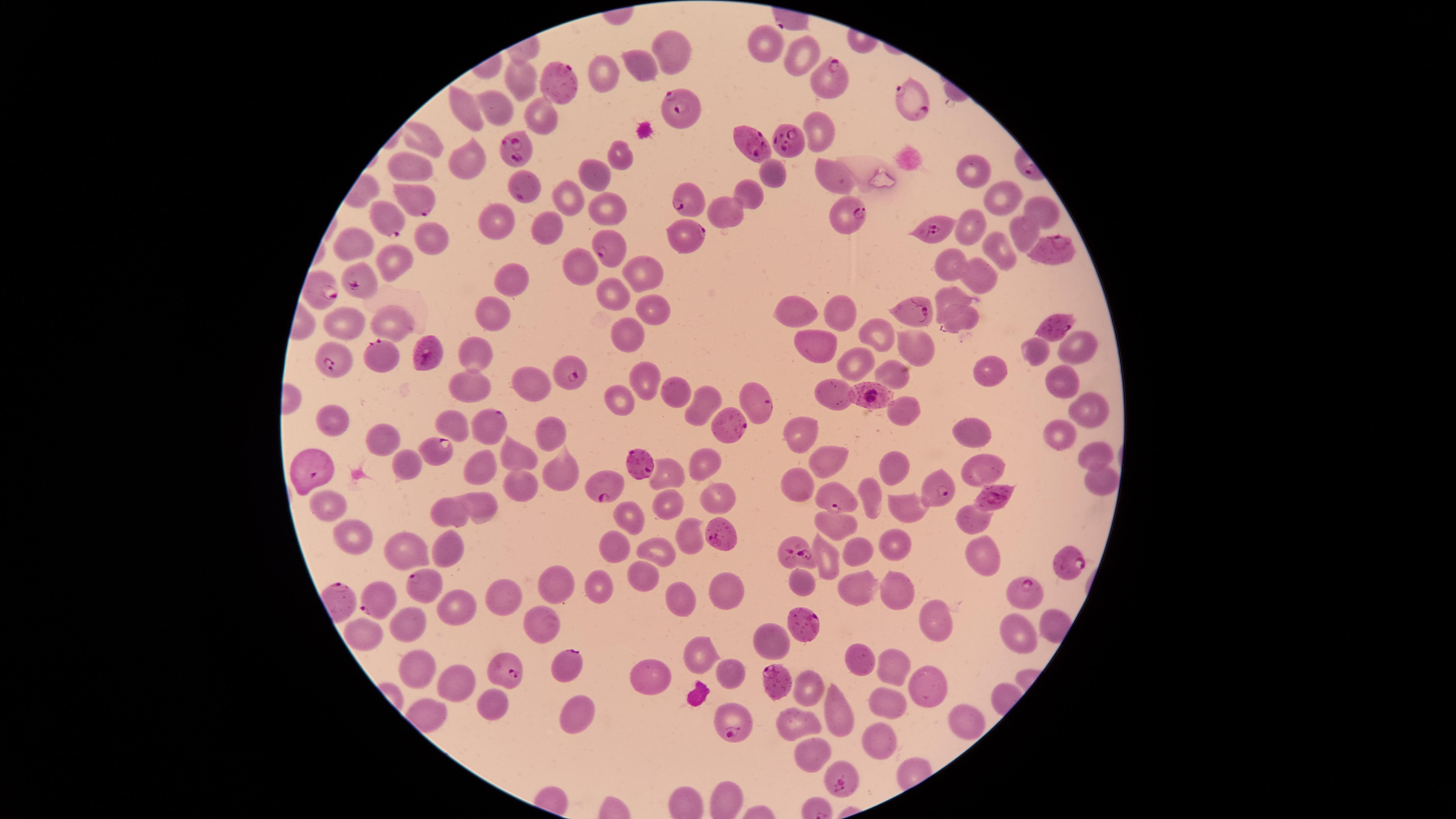
Approximate marker points as {x, y} in pixels.
Summary:
  - Uninfected red blood cells: {762, 44}, {672, 49}, {795, 50}, {638, 66}, {601, 74}, {520, 80}, {466, 110}, {493, 111}, {537, 113}, {818, 131}, {425, 140}, {619, 152}, {464, 158}, {413, 163}, {595, 171}, {968, 171}, {774, 172}, {826, 173}, {750, 193}, {566, 200}, {1003, 200}, {610, 206}, {728, 212}, {1040, 212}, {489, 222}, {547, 226}, {972, 226}, {1023, 228}, {352, 236}, {434, 241}, {1002, 248}, {393, 260}, {944, 262}, {580, 265}, {642, 271}, {980, 277}, {518, 278}, {602, 288}, {947, 295}, {656, 309}, {796, 312}, {834, 312}, {348, 318}, {494, 320}, {961, 323}, {394, 325}, {880, 334}, {634, 335}, {1072, 344}, {815, 346}, {912, 347}, {1036, 349}, {475, 358}, {846, 362}, {993, 368}, {887, 370}, {523, 378}, {469, 381}, {645, 381}, {1054, 383}, {674, 386}, {838, 390}, {616, 396}, {905, 405}, {697, 407}, {1093, 409}, {334, 415}, {449, 418}, {387, 433}, {976, 434}, {801, 435}, {550, 438}, {1063, 438}, {518, 454}, {1089, 456}, {828, 461}, {703, 463}, {980, 463}, {408, 465}, {558, 465}, {479, 467}, {890, 470}, {657, 476}, {1091, 481}, {518, 482}, {797, 484}, {867, 486}, {672, 498}, {717, 498}, {331, 501}, {483, 506}, {908, 507}, {451, 514}, {632, 518}, {972, 522}, {835, 530}, {357, 531}, {686, 539}, {401, 542}, {893, 544}, {448, 546}, {613, 546}, {653, 550}, {976, 555}, {857, 556}, {826, 562}, {642, 577}, {804, 581}, {601, 586}, {861, 588}, {896, 588}, {557, 590}, {726, 594}, {505, 597}, {680, 598}, {456, 612}, {933, 616}, {408, 621}, {541, 621}, {1017, 624}, {364, 630}, {768, 639}, {702, 652}, {864, 662}, {890, 663}, {730, 671}, {415, 674}, {646, 676}, {452, 684}, {932, 684}, {808, 694}, {887, 702}, {572, 714}, {838, 716}, {794, 721}, {961, 723}, {879, 741}, {809, 759}
  - Parasitized red blood cells: {559, 78}, {830, 82}, {914, 101}, {682, 104}, {789, 139}, {751, 140}, {518, 147}, {528, 194}, {685, 196}, {417, 199}, {389, 217}, {847, 218}, {930, 228}, {686, 234}, {1047, 247}, {607, 250}, {362, 277}, {319, 286}, {911, 309}, {1050, 324}, {384, 358}, {419, 358}, {347, 359}, {572, 377}, {880, 394}, {761, 400}, {495, 416}, {730, 422}, {441, 450}, {642, 460}, {317, 471}, {612, 487}, {942, 495}, {991, 498}, {843, 500}, {719, 530}, {797, 557}, {1069, 564}, {422, 588}, {345, 597}, {1026, 598}, {384, 602}, {797, 627}, {569, 665}, {502, 674}, {783, 685}, {742, 727}, {847, 783}
  - Preparation: thin blood film
  - Field of view: single
  - Species: Plasmodium falciparum
  - Presence: malaria parasites identified
  - Image size: 1456×819 pixels
  - Visible region: circular
  - Capture: smartphone photograph through the microscope eyepiece
  - Stain: Giemsa